Locate every Plasmodium falciparum parasite and give its life-cycle stage, and locate every leukocyte and any debris.
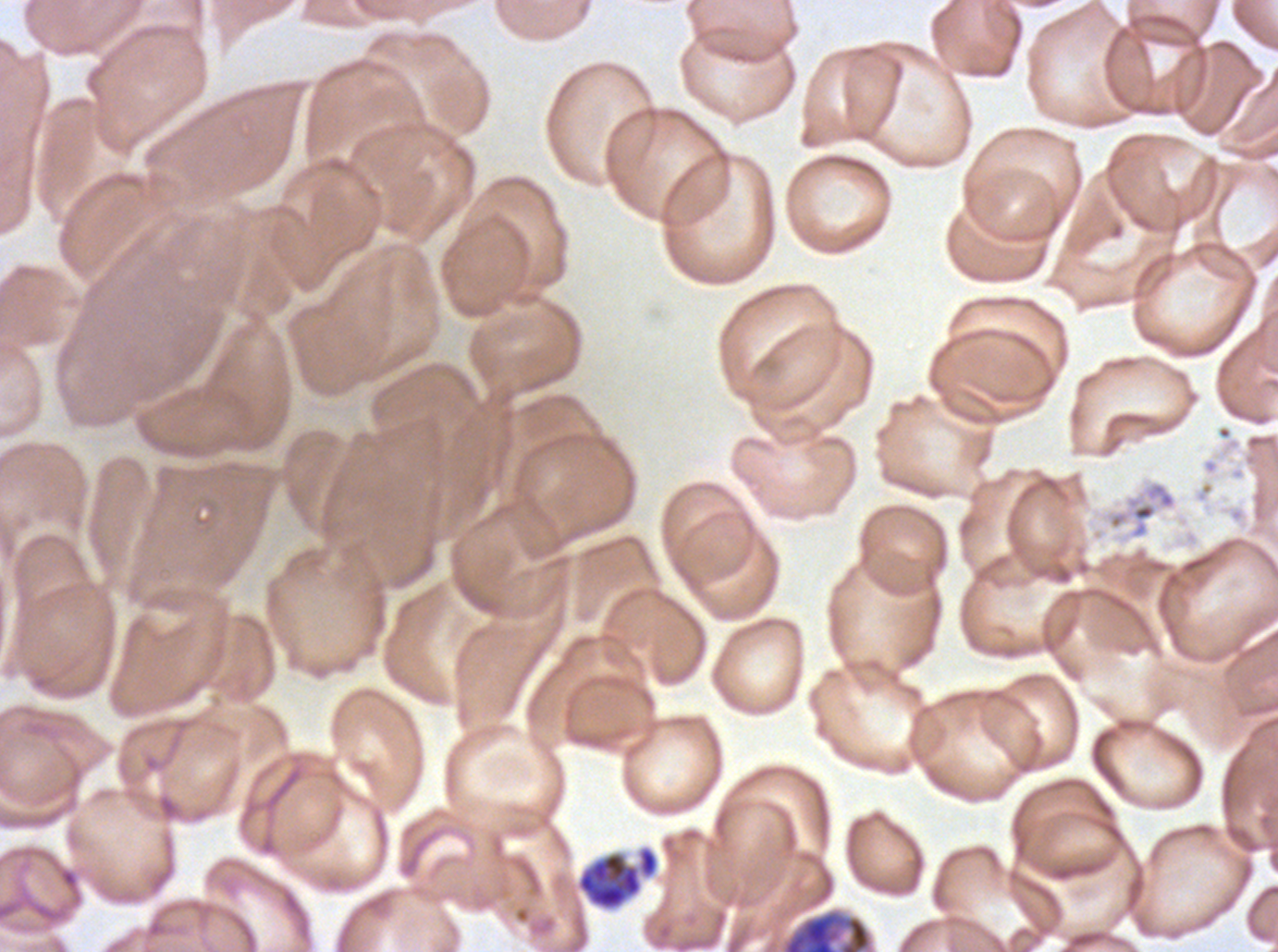
Approximate bounding rectangles given as corner coordinates in pixels from the top-left.
Early schizonts: (x1=576, y1=846, x2=658, y2=910), (x1=780, y1=908, x2=874, y2=951).
Debris: (x1=1100, y1=479, x2=1178, y2=541).
No rings, late-ring/early-trophozoite forms, mid trophozoites, late trophozoites, late schizonts, segmenters, gametocytes, or leukocytes observed.

Summary:
  - Preparation: thin blood smear
  - Image size: 1278×952 pixels
  - Stain: Giemsa
  - Specimen: Plasmodium falciparum from a patient in The Gambia, cultured ex vivo for 24 to 48 hours
  - Field of view: sub-image separated from a larger composite